Assess this cell for malaria.
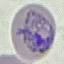

Parasitized.

Summary:
  - Image type: automatically extracted cell patch, resized to 64 × 64 pixels
  - Capture: smartphone camera at the microscope eyepiece
  - Stain: Giemsa
  - Preparation: thin blood smear